Locate every malaria parasite and every leukocyte.
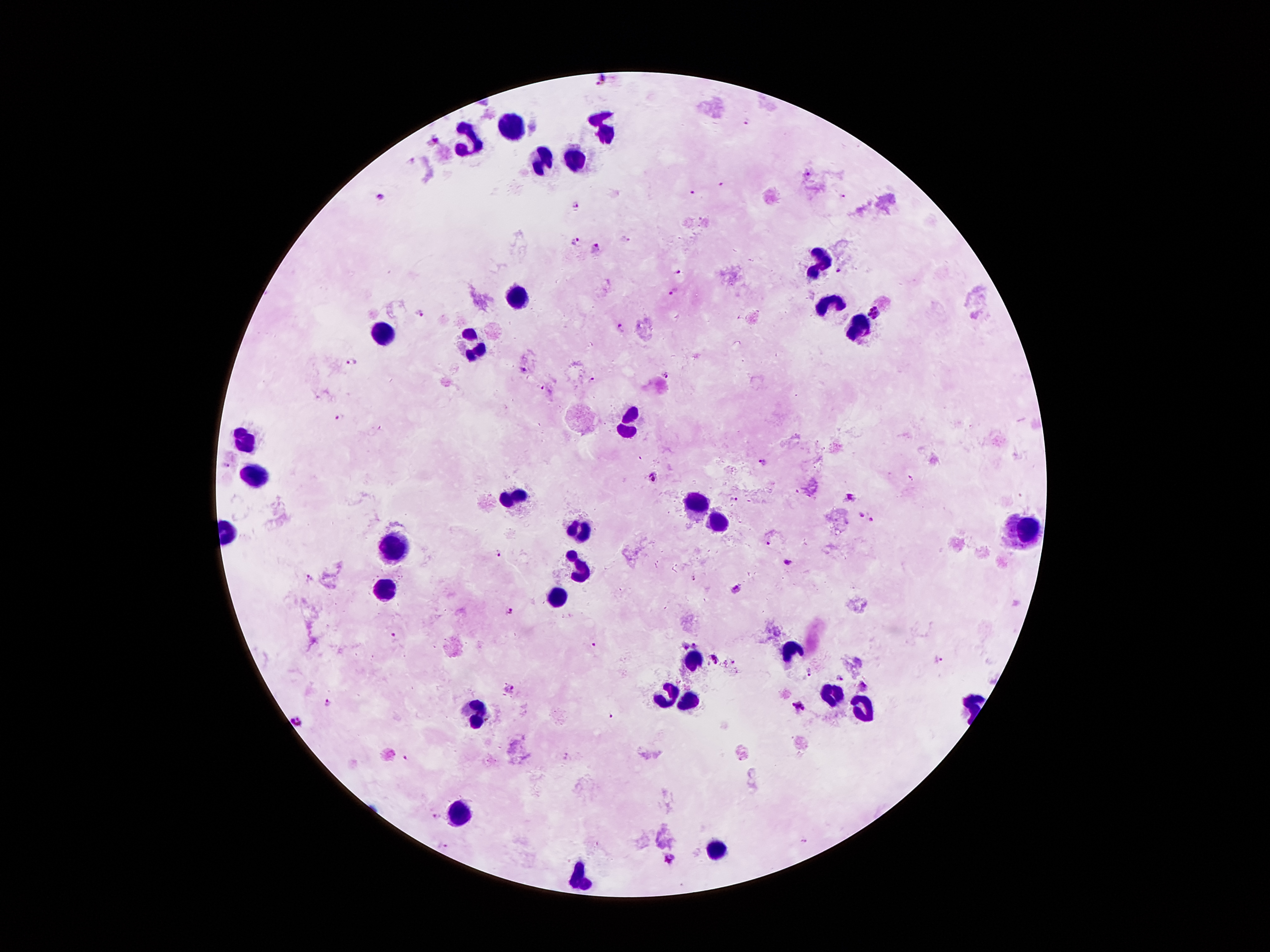
Approximate centers as (x, y) in pixels.
Malaria parasites: (599, 78), (747, 124), (434, 139), (412, 158), (720, 182), (693, 194), (380, 198), (841, 198), (578, 205), (625, 238), (576, 241), (596, 246), (679, 270), (837, 270), (673, 290), (421, 312), (874, 313), (619, 326), (353, 360), (521, 369), (664, 374), (592, 377), (541, 386), (340, 414), (763, 461), (223, 467), (653, 474), (847, 495), (861, 514), (871, 517), (767, 542), (499, 552), (785, 561), (310, 578), (737, 591), (506, 610), (392, 632), (594, 643), (695, 646), (685, 647), (714, 657), (939, 661), (809, 673), (839, 677), (864, 686), (508, 689), (327, 703), (797, 704), (614, 716), (299, 723), (407, 757), (438, 817), (671, 861).
Leukocytes: (602, 121), (510, 127), (467, 143), (578, 158), (543, 166), (819, 260), (512, 301), (823, 303), (858, 324), (383, 334), (473, 344), (629, 420), (246, 439), (256, 473), (516, 498), (692, 504), (719, 523), (1032, 523), (580, 529), (387, 547), (580, 568), (387, 588), (555, 596), (790, 650), (692, 660), (827, 690), (663, 695), (688, 701), (862, 711), (473, 715), (461, 813), (713, 848), (580, 877).

Summary:
  - Capture: smartphone camera through the microscope eyepiece
  - Image size: 1270×952 pixels
  - Magnification: 100x
  - Preparation: thick blood smear
  - Stain: Giemsa
  - Patient malaria status: positive for Plasmodium falciparum
  - Field of view: single